Assess this cell for malaria.
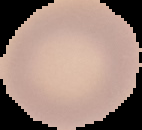
It is uninfected.

Summary:
  - Preparation: thin blood film
  - Image type: cell region segmented out of the field of view; surrounding area masked to black
  - Image size: 142×130 pixels